Assess this cell for malaria.
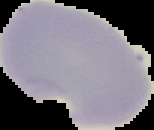
It is parasitized.

preparation = thin blood smear
image size = 154×130 pixels
image type = segmented cell region with the area outside set to black